Outline platelets.
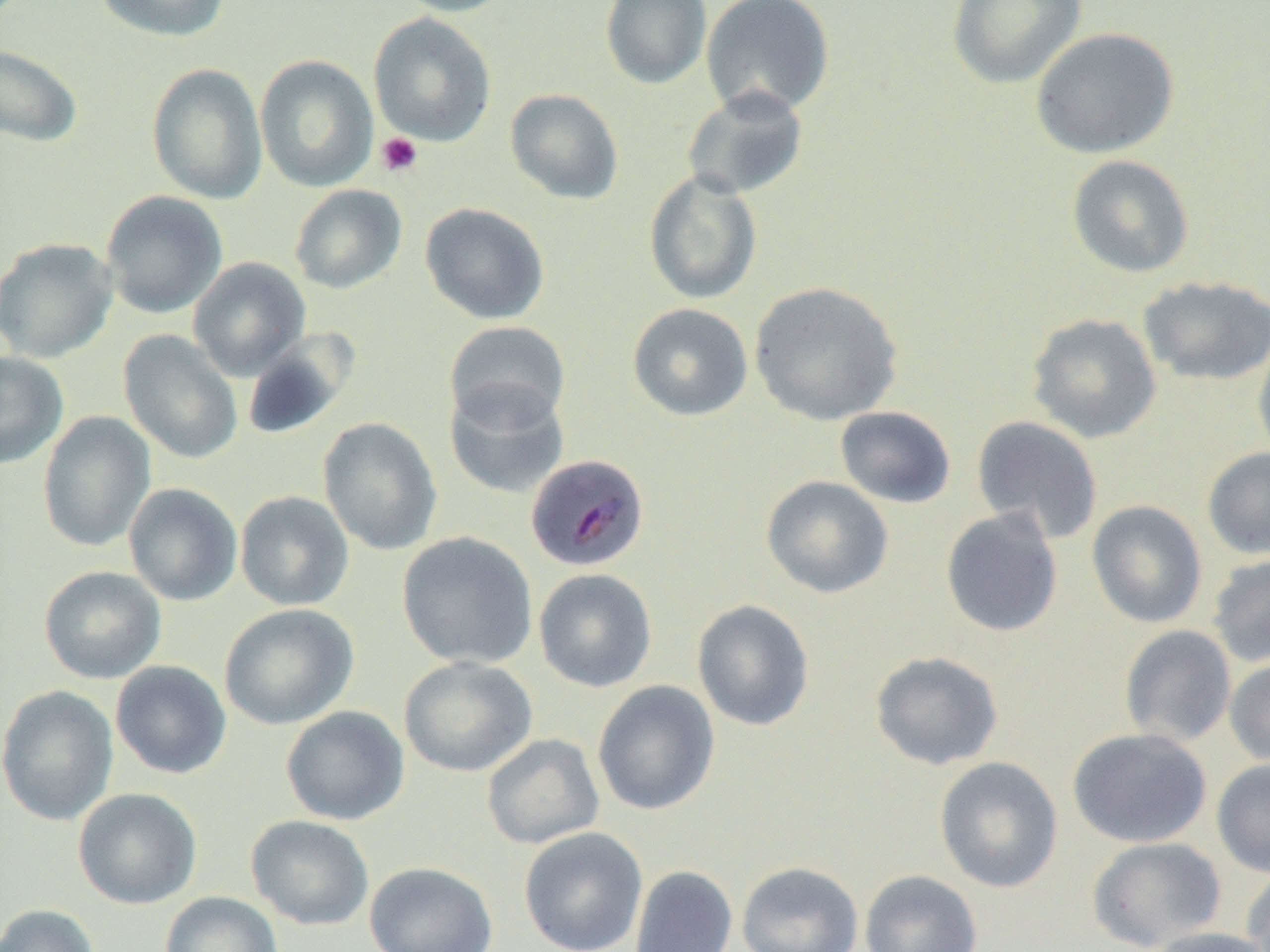
Approximate bounding boxes as (x1, y1, x2, y2) in pixels.
Platelets: (375, 132, 423, 177).

slide_level_diagnosis: Plasmodium malariae
field_of_view: one of a larger specimen
magnification: 1000x
uninfected_red_blood_cell_locations: 'approximate bounding boxes as (x1, y1, x2, y2) in pixels: (93, 0, 231, 43), (390, 0, 517, 17), (600, 0, 712, 90), (701, 0, 835, 118), (946, 0, 1087, 89), (369, 13, 497, 146), (1030, 27, 1179, 159), (0, 44, 83, 147), (255, 54, 378, 192), (146, 62, 267, 203), (681, 86, 810, 201), (504, 88, 624, 204), (1066, 155, 1194, 278), (643, 170, 763, 304), (289, 184, 407, 294), (100, 191, 228, 319), (420, 202, 550, 325), (0, 238, 118, 363), (188, 257, 311, 380), (1137, 276, 1270, 387), (748, 281, 904, 426), (627, 303, 753, 422), (1026, 312, 1162, 443), (444, 321, 571, 430), (240, 329, 359, 442), (119, 330, 243, 464), (1253, 331, 1270, 467), (0, 351, 68, 469), (444, 381, 569, 499), (834, 406, 956, 508), (37, 411, 156, 552), (971, 415, 1104, 544), (318, 417, 443, 555), (1202, 447, 1270, 560), (761, 476, 894, 598), (123, 483, 243, 606), (234, 491, 354, 610), (1086, 500, 1208, 628), (940, 507, 1063, 637), (396, 531, 538, 669), (1206, 554, 1270, 668), (38, 566, 166, 684), (534, 568, 657, 692), (692, 599, 814, 731), (218, 603, 359, 730), (1119, 624, 1236, 747), (869, 650, 1004, 770), (398, 656, 538, 777), (1224, 656, 1270, 768), (111, 660, 232, 779), (592, 680, 720, 816), (0, 684, 119, 826), (281, 706, 410, 825), (1067, 727, 1212, 848), (481, 733, 605, 849), (934, 756, 1064, 893), (1211, 759, 1270, 878), (73, 787, 202, 909), (246, 815, 374, 930), (518, 826, 648, 952), (1087, 836, 1226, 951), (363, 861, 498, 952), (736, 861, 864, 952), (629, 864, 738, 952), (1240, 867, 1270, 951), (859, 869, 983, 952), (159, 891, 283, 952), (0, 903, 100, 952), (1147, 926, 1270, 952)'
image_size: 1270×952 pixels
preparation: thin blood smear
modality: optical microscopy
plasmodium_malariae_infected_red_blood_cell_locations: 'approximate bounding boxes as (x1, y1, x2, y2) in pixels: (525, 454, 650, 572)'